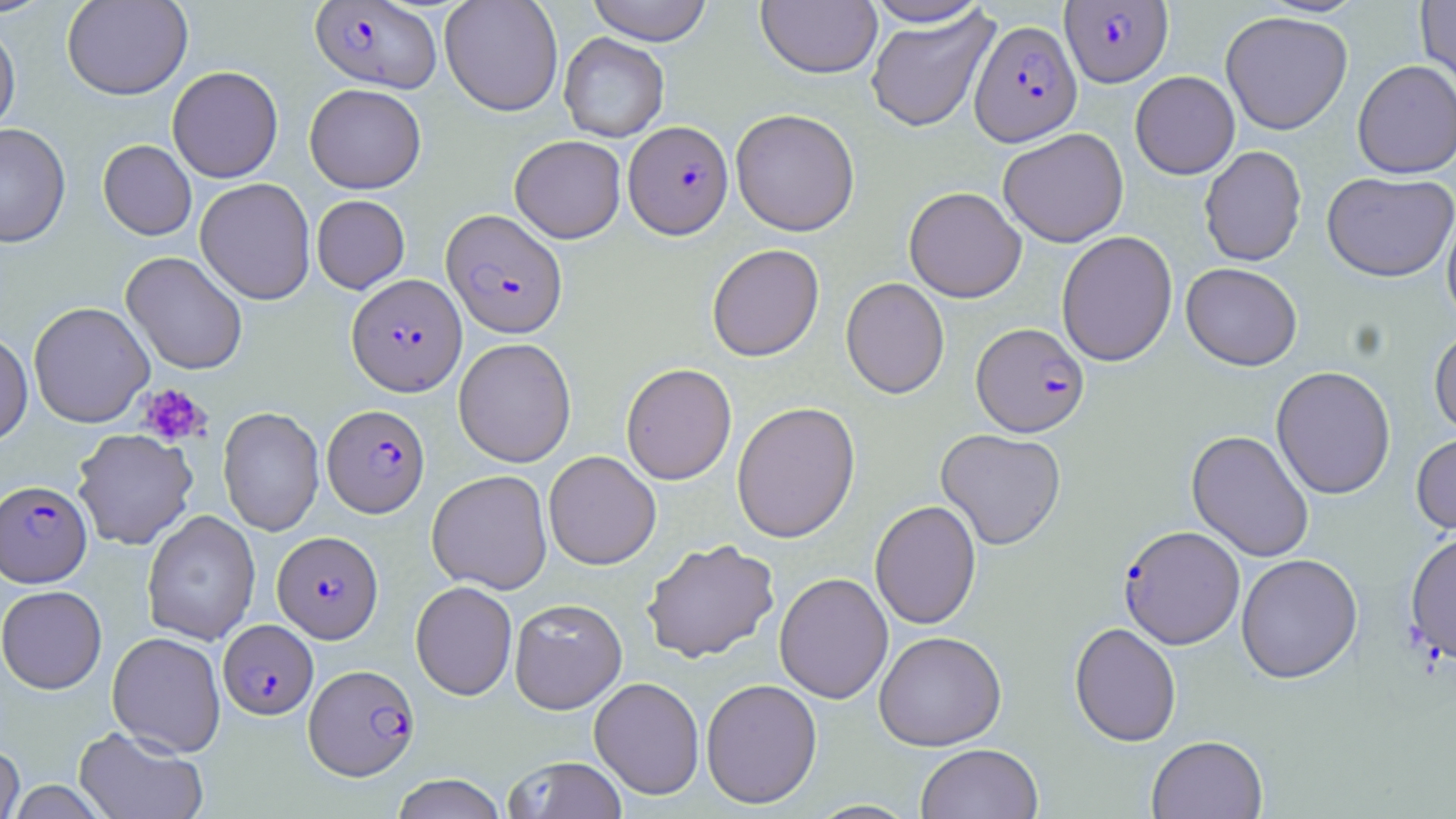
Approximate bounding boxes as (x1,y1)-(x2,y2) corner pairs in pixels. Plasmodium falciparum-infected red blood cell locations: (310,1)-(441,93), (1061,1)-(1173,87), (970,20)-(1081,145), (624,120)-(733,239), (441,209)-(567,338), (346,274)-(466,395), (971,322)-(1090,437), (322,404)-(430,518), (0,480)-(92,587), (1119,525)-(1245,649), (272,530)-(383,643), (218,620)-(318,720), (305,664)-(419,780). Platelet locations: (137,383)-(210,447). Uninfected red blood cell locations: (61,0)-(192,100), (440,0)-(564,116), (586,0)-(713,45), (862,0)-(994,27), (1416,0)-(1456,94), (756,1)-(882,78), (866,10)-(998,132), (1220,11)-(1353,135), (0,20)-(20,138), (559,32)-(669,142), (1352,60)-(1456,178), (167,65)-(283,183), (1130,71)-(1240,179), (304,83)-(426,193), (731,108)-(860,236), (0,123)-(71,248), (998,128)-(1128,247), (510,135)-(626,243), (98,140)-(196,240), (1199,146)-(1307,266), (1322,170)-(1456,282), (195,177)-(316,305), (903,186)-(1027,303), (312,195)-(410,293), (1441,203)-(1456,328), (1056,230)-(1178,366), (707,243)-(824,361), (121,251)-(248,375), (1181,262)-(1303,370), (840,277)-(949,399), (28,301)-(154,428), (1429,326)-(1456,438), (0,329)-(33,448), (453,337)-(577,467), (621,363)-(737,485), (1271,365)-(1396,499), (732,401)-(861,542), (218,407)-(324,536), (72,428)-(198,550), (935,428)-(1066,550), (1187,429)-(1314,562), (1411,431)-(1456,537), (543,450)-(661,570), (426,469)-(552,593), (869,500)-(982,630), (142,510)-(260,645), (1404,527)-(1456,667), (642,539)-(780,663), (1235,553)-(1363,683), (774,572)-(893,703), (410,581)-(517,700), (1,585)-(106,693), (509,598)-(627,714), (1069,622)-(1182,746), (874,630)-(1006,750), (107,631)-(226,757), (589,676)-(705,799), (700,678)-(822,808), (74,725)-(208,819), (1146,734)-(1268,819), (0,742)-(24,819), (915,743)-(1043,819), (503,756)-(627,819), (390,773)-(506,819). Slide-level diagnosis: Plasmodium falciparum. Optical microscopy. 1000x magnification. Image is 1456×819 pixels. One field of a larger specimen. May-Grünwald-Giemsa-stained preparation. Thin blood smear.